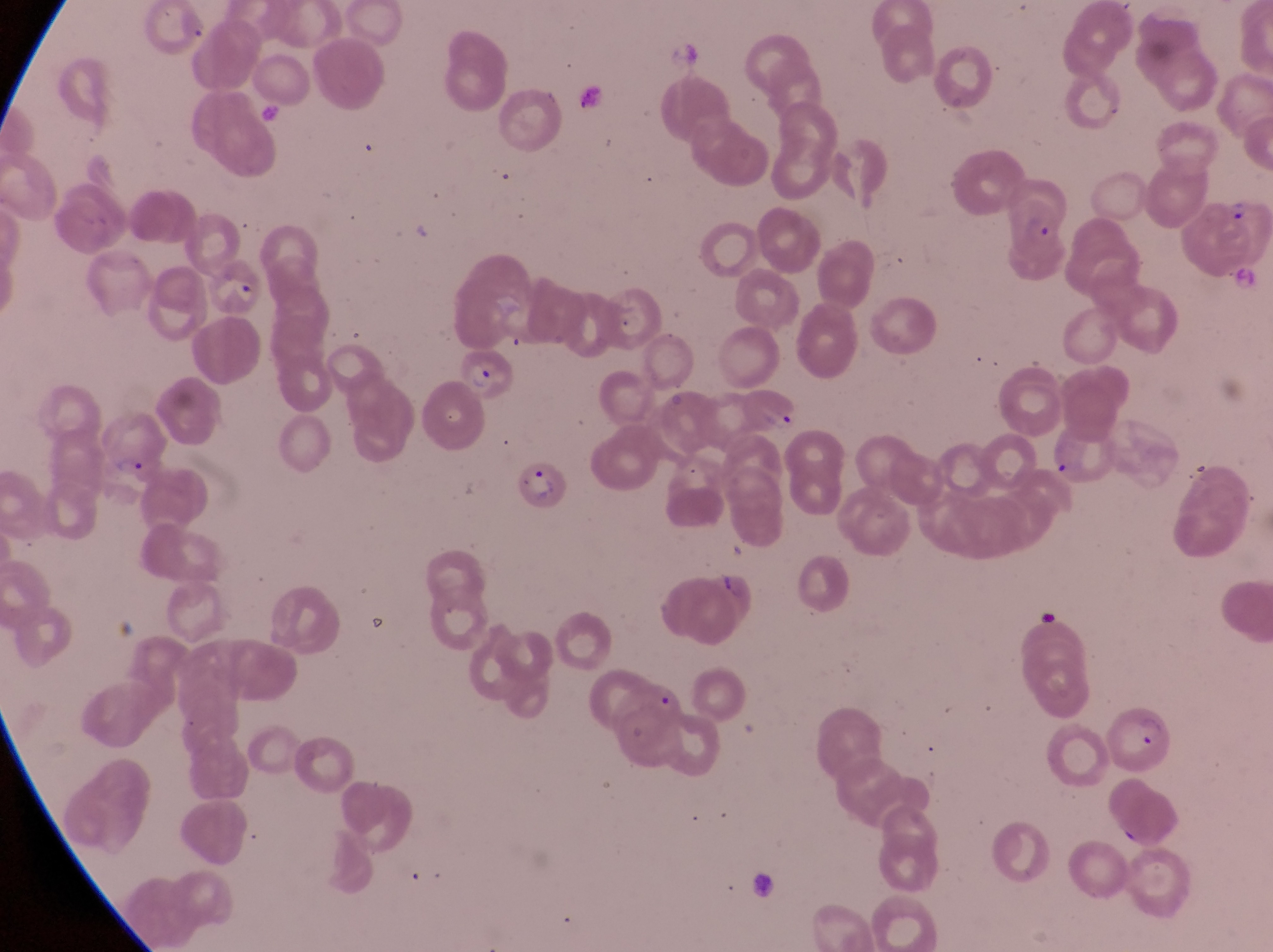
magnification = 1000x
country = Uganda
parasitised red blood cell locations = approximate bounding boxes as left top right bottom in pixels: 1006 172 1076 259; 202 250 265 315; 454 344 526 401; 734 384 806 437; 514 459 569 517; 1103 700 1173 778
preparation = thin blood smear
artifact (platelet-like body, stain precipitate, or debris) locations = approximate bounding boxes as left top right bottom in pixels: 1233 259 1263 291; 709 569 739 599
field of view = single
capture = smartphone photograph through the eyepiece of an Olympus CX-23 microscope
image size = 1273×952 pixels
trophozoite locations = approximate bounding boxes as left top right bottom in pixels: 1228 197 1255 225; 112 452 145 480